State which parasite is depicted.
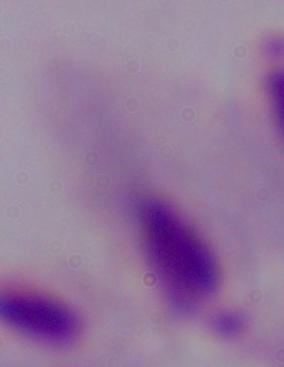
A trichomonad.

modality: micrograph
magnification: 1000x